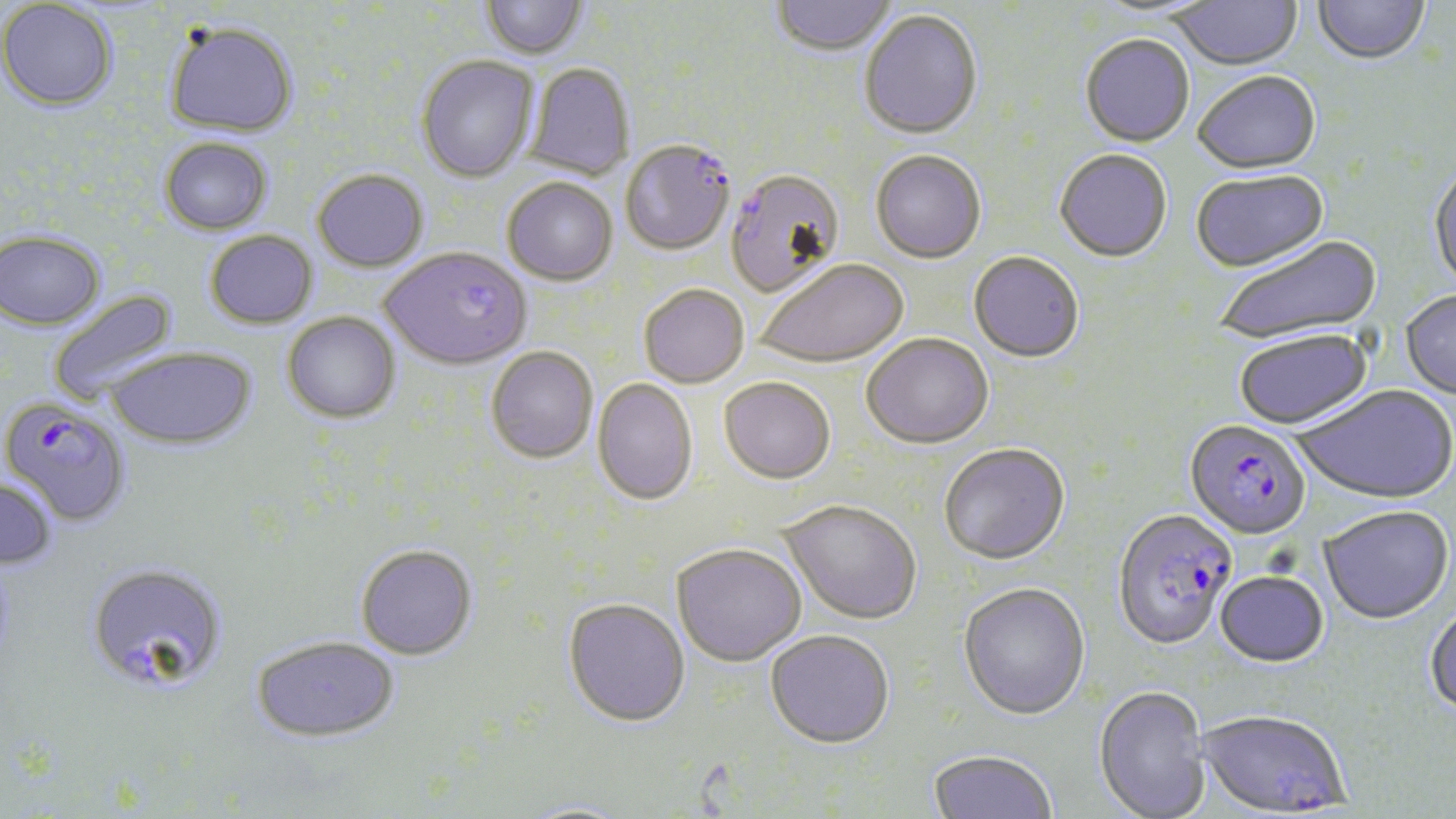
Summary:
  - Coordinate format: approximate bounding boxes as (x1, y1, x2, y2) in pixels
  - Uninfected red blood cell locations: (480, 0, 588, 61), (772, 0, 896, 58), (1173, 0, 1301, 72), (1313, 0, 1430, 68), (1, 1, 118, 111), (1088, 1, 1219, 23), (859, 11, 984, 142), (164, 21, 299, 137), (1080, 36, 1195, 149), (416, 56, 539, 184), (524, 64, 636, 181), (1192, 73, 1322, 177), (158, 137, 273, 234), (1054, 151, 1172, 265), (871, 152, 986, 266), (1428, 165, 1456, 296), (312, 170, 429, 273), (725, 171, 845, 299), (1192, 172, 1331, 276), (502, 180, 618, 287), (0, 229, 106, 330), (204, 230, 318, 329), (1215, 236, 1384, 347), (383, 248, 532, 372), (968, 254, 1084, 365), (755, 260, 909, 370), (639, 286, 749, 390), (47, 288, 180, 406), (1401, 292, 1456, 401), (282, 312, 401, 424), (1234, 332, 1374, 432), (861, 336, 994, 451), (106, 347, 256, 449), (486, 347, 598, 464), (592, 379, 698, 507), (718, 379, 835, 487), (1293, 386, 1456, 507), (939, 445, 1070, 567), (0, 477, 58, 570), (779, 502, 922, 628), (1318, 508, 1454, 627), (355, 545, 478, 663), (671, 545, 806, 669), (86, 562, 228, 695), (1214, 573, 1330, 671), (958, 584, 1090, 723), (562, 600, 690, 729), (1424, 604, 1456, 721), (765, 632, 894, 752), (251, 636, 400, 744), (1093, 688, 1211, 819), (927, 752, 1057, 818)
  - Plasmodium falciparum-infected red blood cell locations: (620, 142, 736, 256), (1, 396, 131, 527), (1184, 422, 1312, 543), (1112, 511, 1237, 653), (1197, 712, 1350, 817)
  - Slide-level diagnosis: Plasmodium falciparum
  - Preparation: thin blood smear
  - Image size: 1456×819 pixels
  - Field of view: single
  - Stain: May-Grünwald-Giemsa
  - Modality: light microscopy
  - Magnification: 1000x